Point out each Plasmodium parasite.
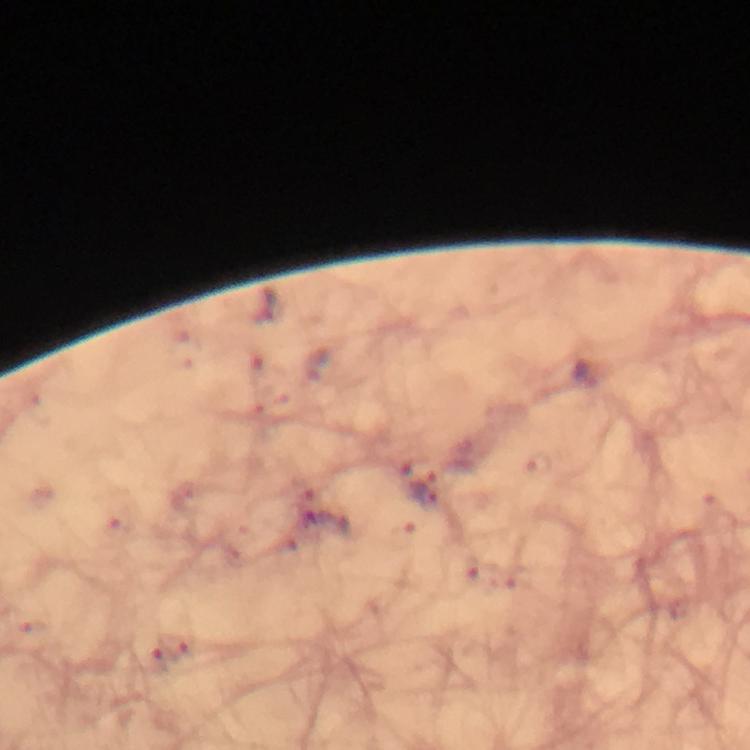

Approximate object centers, in pixels from the top-left corner.
Plasmodium parasites: (x=425, y=495).

Summary:
  - Cropped from: one field of view
  - Image size: 750×750 pixels
  - Stain: Giemsa
  - Immersion oil: applied
  - Magnification: 100x
  - Preparation: thick blood film
  - Context: from a diagnostic examination for malaria
  - Capture: smartphone mounted on the microscope